Name the cell type shown.
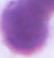

This is an erythrocyte.

Captured at 1000x magnification. Photomicrograph.